Comment on the morphology of the red blood cells.
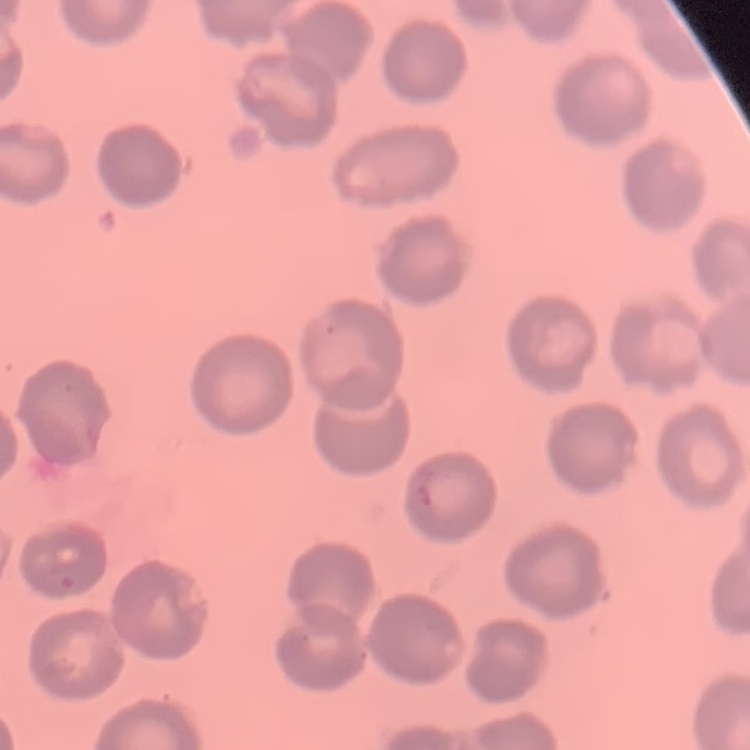

They show no rouleaux formation.

Stained with either Field's or Giemsa. Thin blood smear. Square crop of a larger photomicrograph.